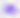 Toxoplasma gondii is seen. 400x magnification. Photomicrograph.